Give the position of every leukocyte visible.
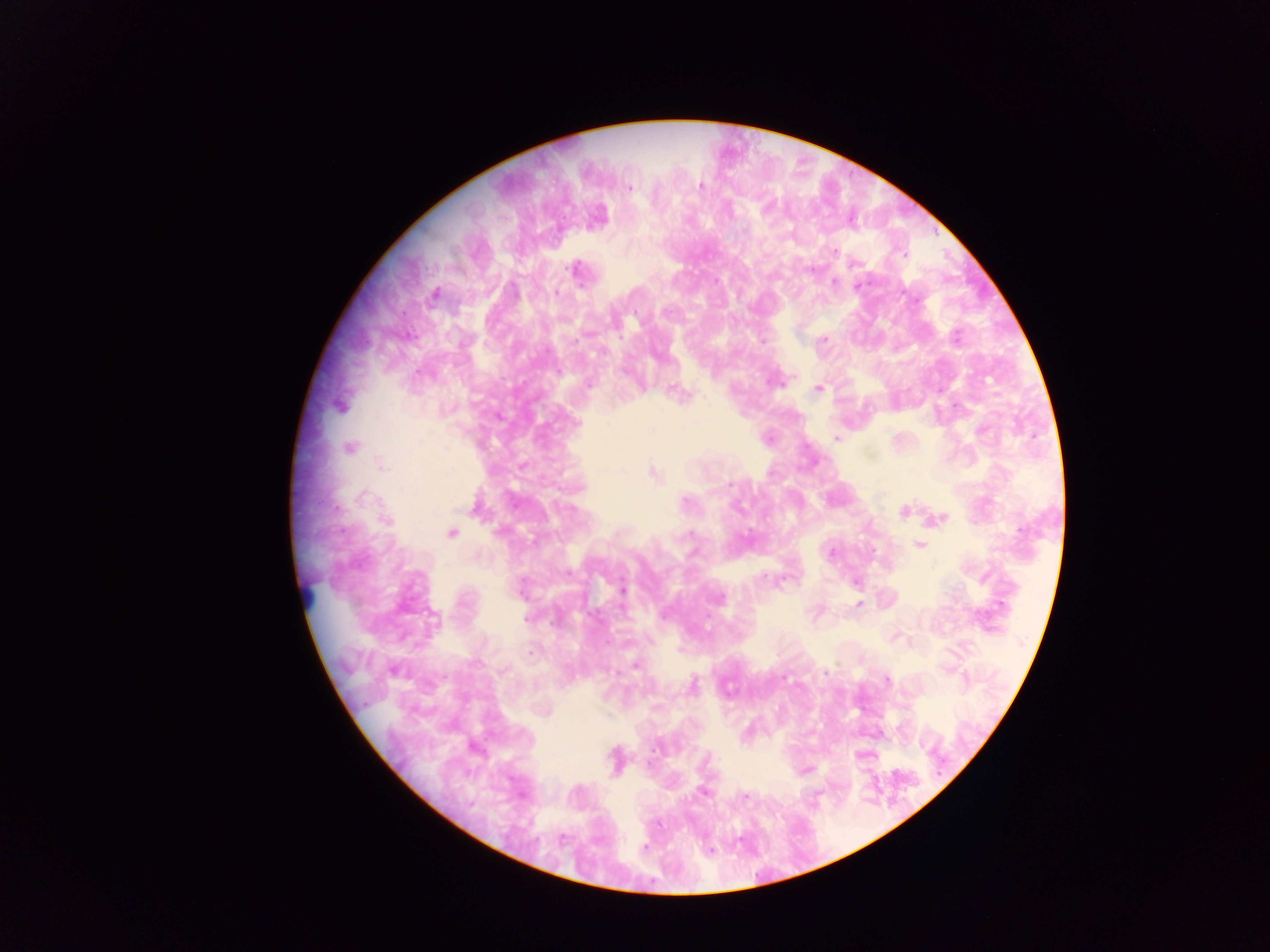
No leukocytes observed.

preparation = thick blood smear
field of view = single
image size = 1270×952 pixels
capture = mobile-phone photograph through a microscope
country = Ghana
malaria parasite locations = approximate centers as {x, y} in pixels: {701, 186}, {628, 187}, {730, 211}, {601, 214}, {834, 251}, {576, 271}, {953, 337}, {762, 338}, {825, 340}, {818, 389}, {686, 393}, {836, 439}, {732, 484}, {833, 551}, {764, 577}, {855, 581}, {621, 589}, {858, 605}, {635, 664}, {828, 671}, {786, 677}, {886, 682}, {658, 747}, {703, 791}, {747, 800}, {560, 841}, {644, 845}, {709, 848}